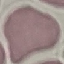
Result: no malaria parasites seen. Acquired by smartphone through the microscope eyepiece. Thin blood film. Automatically extracted cell patch, resized to 64 × 64 pixels. Giemsa-stained preparation.